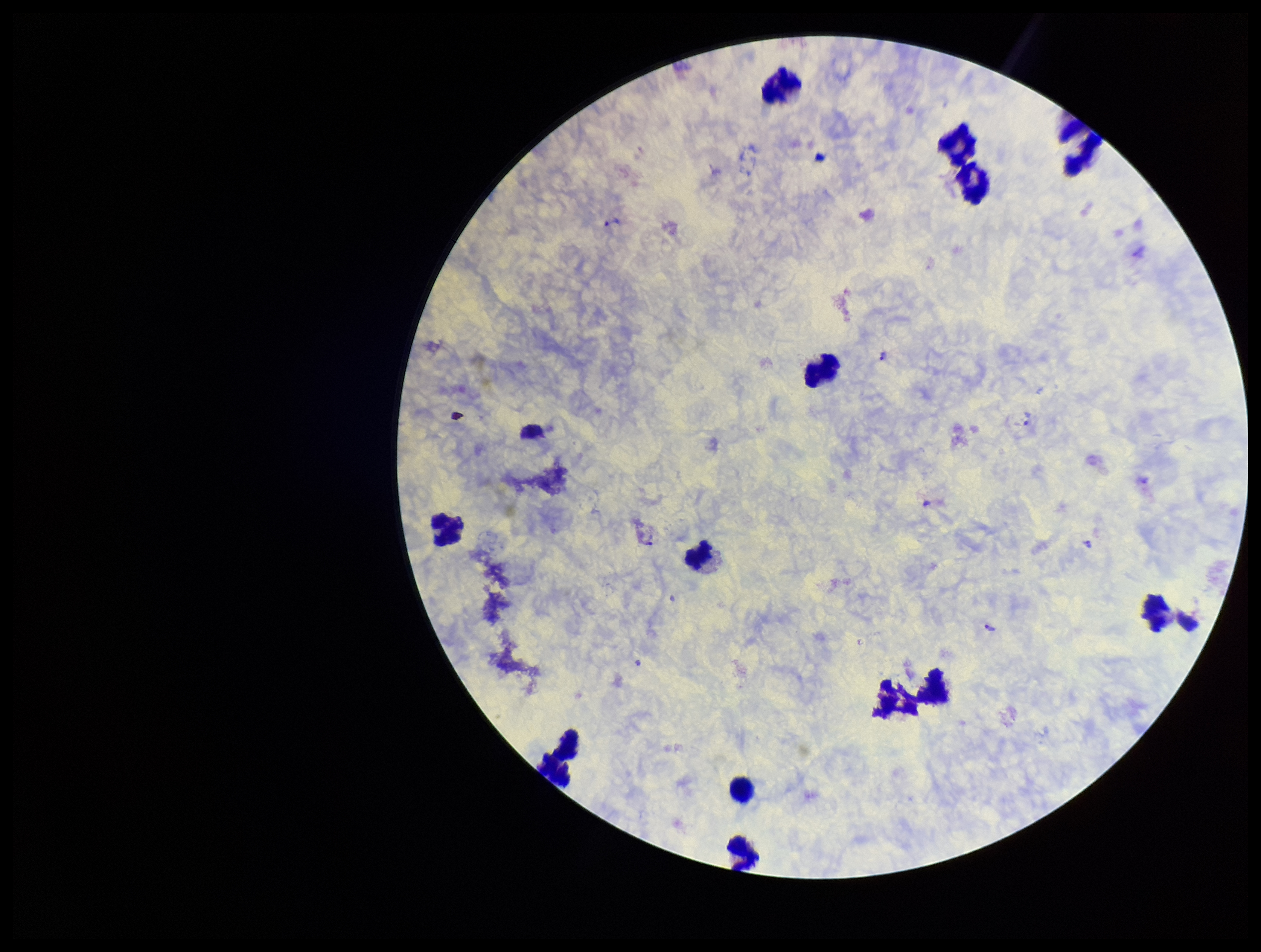
Parasite count: 5. Species reported for this patient: Plasmodium vivax. Image is 1261×952 pixels. Giemsa stain. Leukocyte count: 13. One field from this slide. Preparation: thick. Patient malaria status: infected. Plasmodium parasites: seen. Photographed through the microscope eyepiece with a smartphone camera.